Comment on the morphology of the red blood cells.
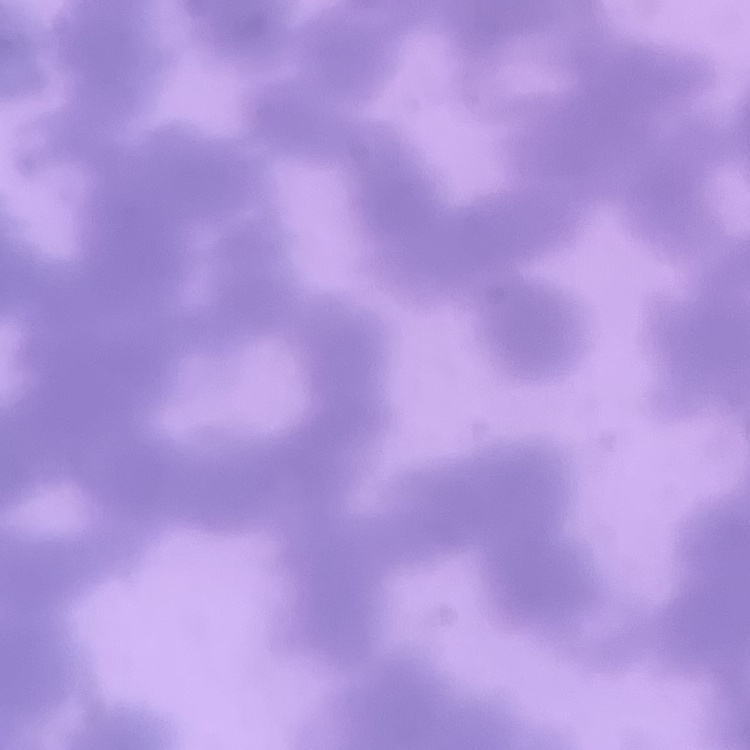
Rouleaux formation.

Summary:
  - Preparation: thin blood smear
  - Image type: square crop of a larger photomicrograph
  - Stain: Field's or Giemsa